Report the malaria status of this cell.
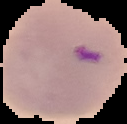

Parasitized.

Summary:
  - Image type: segmented cell region with the area outside set to black
  - Image size: 127×124 pixels
  - Preparation: thin blood film